Report the malaria status of this cell.
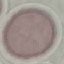
Uninfected.

Summary:
  - Capture: smartphone through the microscope eyepiece
  - Stain: Giemsa
  - Image type: cell patch, automatically extracted from a larger field of view and resized to 64 × 64 pixels
  - Preparation: thin blood film